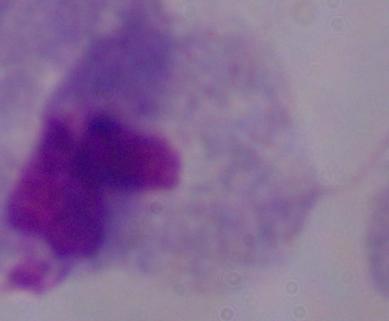
{
  "magnification": "1000x",
  "modality": "micrograph",
  "identification": "trichomonad"
}